Give the extent of all Plasmodium vivax-infected red blood cells.
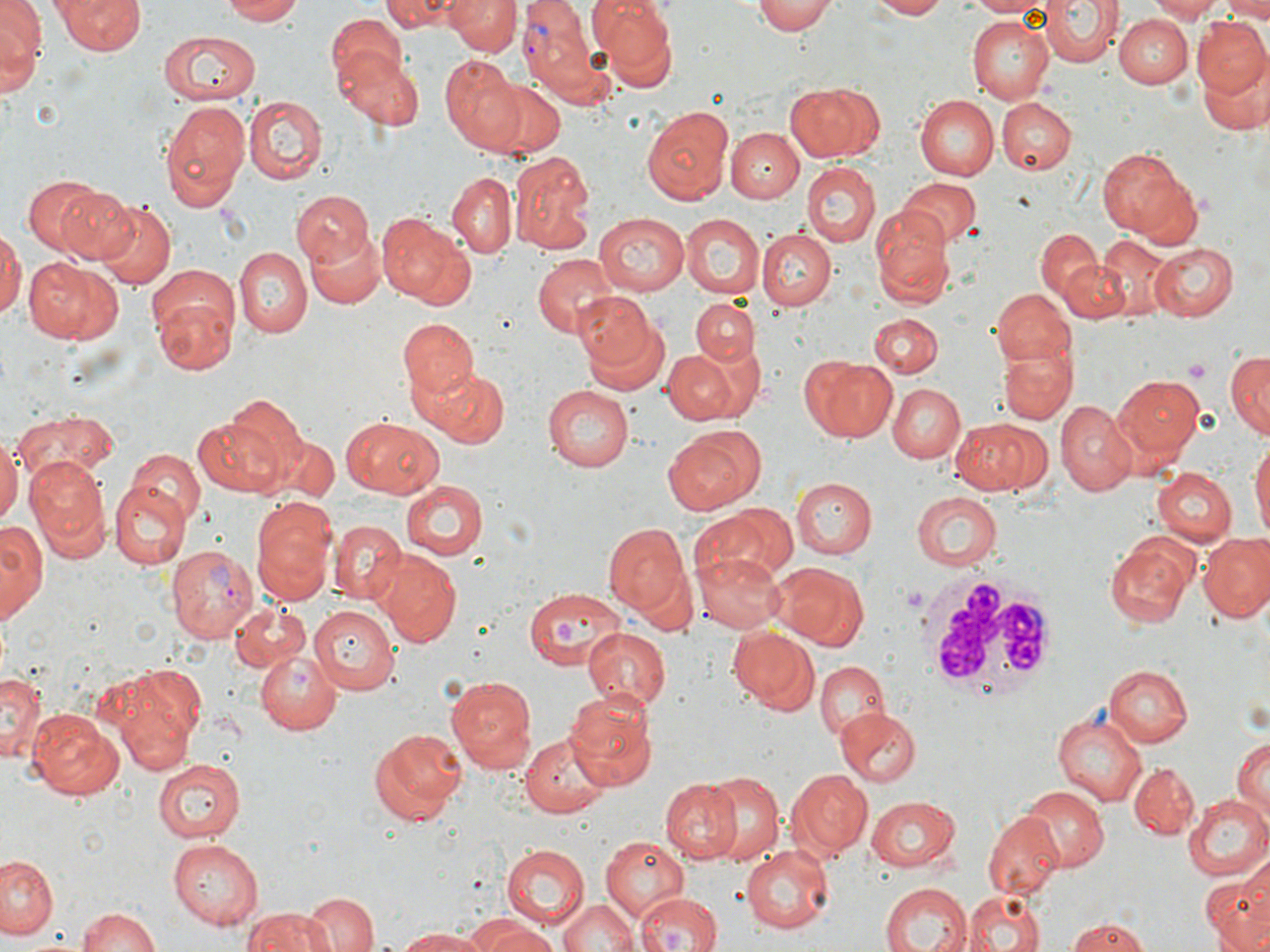
Approximate bounding boxes as (x1,y1)-(x2,y2) corner pairs in pixels.
Plasmodium vivax-infected red blood cells: (521,4)-(606,103), (165,543)-(257,643).

Summary:
  - Uninfected red blood cell locations: (1,0)-(44,81), (54,0)-(144,55), (219,0)-(309,24), (382,0)-(462,30), (445,0)-(519,55), (590,0)-(678,86), (750,0)-(836,35), (866,0)-(954,19), (964,0)-(1054,17), (1040,0)-(1120,68), (1149,0)-(1222,22), (1220,0)-(1270,21), (324,8)-(410,101), (1116,14)-(1189,87), (963,16)-(1054,105), (1191,19)-(1270,98), (159,30)-(261,106), (338,51)-(426,131), (441,56)-(527,153), (1199,57)-(1269,134), (487,78)-(564,157), (785,83)-(880,162), (914,94)-(999,180), (245,96)-(327,183), (997,98)-(1077,173), (160,99)-(249,212), (641,103)-(735,202), (729,128)-(803,202), (1098,145)-(1199,245), (509,151)-(596,252), (802,162)-(878,247), (447,173)-(514,259), (22,175)-(117,262), (900,179)-(980,249), (56,186)-(143,265), (294,189)-(373,266), (94,201)-(175,291), (871,208)-(954,306), (593,212)-(690,295), (677,213)-(764,300), (377,214)-(475,310), (0,225)-(23,322), (305,226)-(387,310), (1035,227)-(1102,306), (759,230)-(835,308), (1095,234)-(1177,320), (1150,241)-(1237,320), (235,247)-(312,341), (532,251)-(614,336), (24,258)-(123,345), (1062,258)-(1130,322), (150,281)-(240,376), (992,289)-(1078,367), (691,295)-(758,365), (676,300)-(760,425), (578,303)-(671,398), (868,313)-(941,377), (398,318)-(478,402), (997,348)-(1076,424), (665,351)-(738,424), (1225,351)-(1270,437), (800,355)-(898,442), (423,366)-(508,449), (1111,372)-(1205,460), (888,384)-(965,463), (543,386)-(635,472), (221,393)-(308,484), (1056,401)-(1137,496), (15,412)-(119,482), (192,413)-(290,497), (341,416)-(444,498), (950,417)-(1051,496), (662,426)-(763,513), (272,432)-(338,504), (1250,435)-(1270,542), (0,437)-(20,526), (126,448)-(205,527), (26,458)-(112,555), (1151,467)-(1237,545), (790,477)-(877,557), (398,480)-(487,559), (109,484)-(190,568), (912,492)-(1001,569), (250,497)-(339,601), (701,502)-(797,583), (0,520)-(45,623), (330,520)-(405,603), (602,524)-(688,616), (1198,533)-(1270,623), (1105,538)-(1198,626), (693,548)-(786,633), (380,553)-(462,646), (774,562)-(869,649), (522,586)-(622,670), (229,598)-(310,673), (309,605)-(399,695), (582,625)-(672,714), (726,627)-(819,716), (255,648)-(344,735), (815,660)-(891,740), (1103,664)-(1192,746), (102,667)-(203,772), (0,669)-(44,763), (446,674)-(537,771), (565,690)-(657,788), (25,707)-(123,802), (1056,709)-(1147,809), (837,710)-(920,786), (369,727)-(467,824), (518,733)-(610,817), (1231,735)-(1270,817), (151,756)-(246,841), (1128,763)-(1198,838), (696,770)-(787,867), (788,770)-(874,856), (660,779)-(742,862), (1020,787)-(1108,870), (1186,793)-(1270,879), (866,795)-(962,869), (984,811)-(1063,898), (599,835)-(690,922), (166,839)-(263,929), (501,844)-(589,926), (741,844)-(834,935), (2,852)-(61,940), (1201,877)-(1270,952), (879,883)-(971,952), (637,891)-(722,952), (965,891)-(1044,951), (303,893)-(377,952), (558,895)-(636,952), (76,905)-(163,952), (239,907)-(328,952), (1065,917)-(1149,951), (475,920)-(559,952), (398,928)-(490,951)
  - White blood cell locations: (917,574)-(1059,699)
  - Platelet locations: (1184,357)-(1212,380), (900,583)-(928,612), (550,617)-(580,650)
  - Slide-level diagnosis: Plasmodium vivax
  - Image size: 1270×952 pixels
  - Field of view: single
  - Magnification: 1000x
  - Preparation: thin blood film
  - Modality: optical microscopy
  - Stain: May-Grünwald-Giemsa